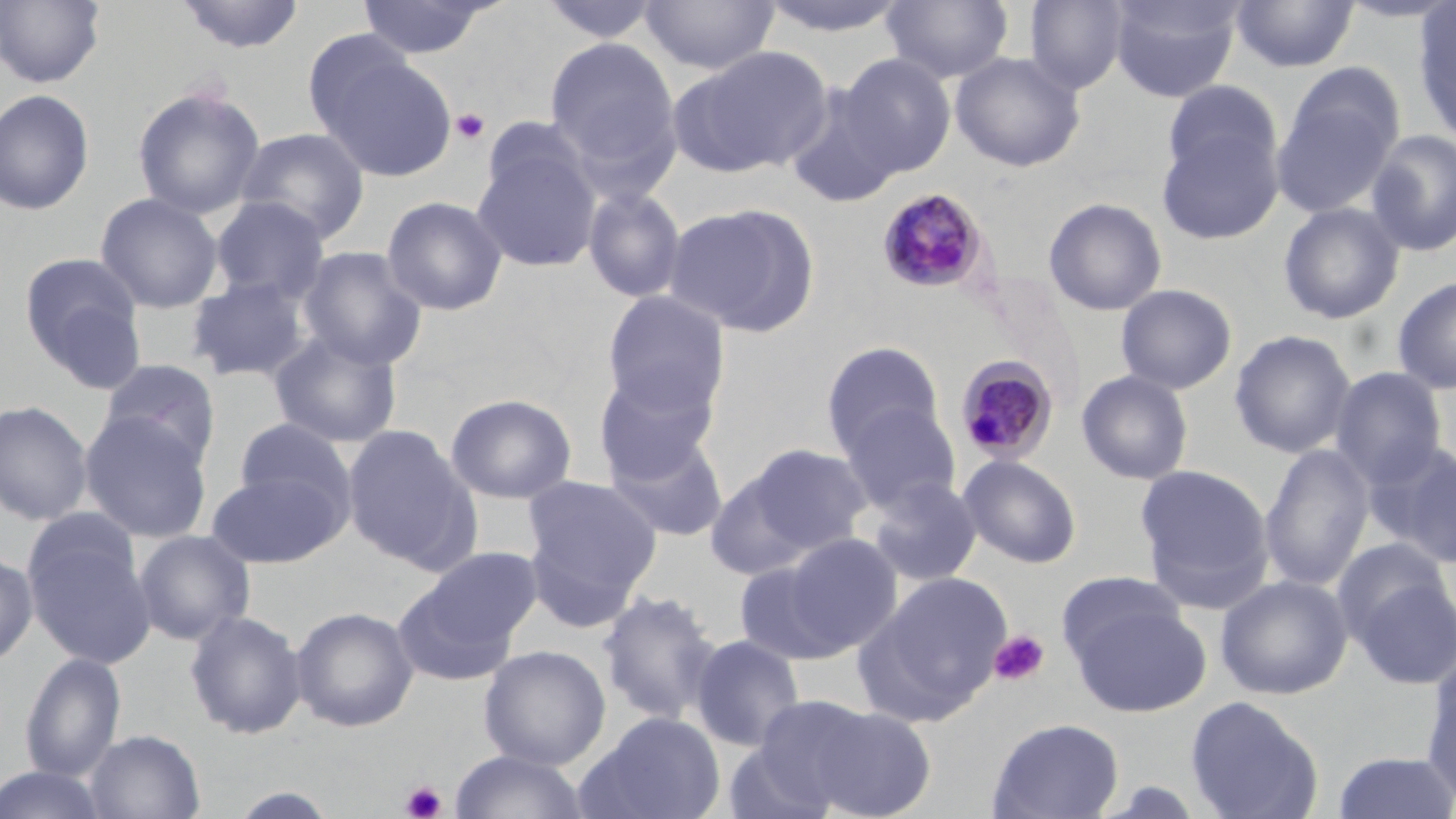

Summary:
  - Coordinate format: approximate bounding boxes as (x1,y1)-(x2,y2) corner pairs in pixels
  - Plasmodium malariae-infected red blood cell locations: (877,187)-(991,294), (954,354)-(1060,465)
  - Uninfected red blood cell locations: (0,0)-(106,88), (173,0)-(307,55), (356,0)-(497,60), (537,0)-(665,45), (640,0)-(780,76), (755,0)-(912,38), (881,0)-(1014,84), (1024,0)-(1130,94), (1108,0)-(1244,103), (1230,0)-(1359,72), (1412,2)-(1456,145), (544,36)-(682,182), (670,45)-(834,178), (319,51)-(458,182), (950,51)-(1086,172), (836,53)-(957,177), (1271,78)-(1400,219), (1160,80)-(1284,189), (131,85)-(266,219), (783,85)-(905,210), (0,89)-(96,215), (1156,121)-(1284,246), (236,126)-(370,243), (1366,129)-(1456,257), (471,137)-(603,273), (581,185)-(687,304), (95,192)-(223,313), (381,195)-(508,316), (210,196)-(329,303), (1043,197)-(1167,316), (664,202)-(821,337), (1278,202)-(1405,324), (298,246)-(429,369), (18,254)-(145,381), (184,275)-(314,385), (1392,276)-(1456,395), (1116,283)-(1238,395), (601,291)-(730,417), (268,330)-(403,449), (1230,330)-(1356,459), (820,340)-(946,459), (98,358)-(220,469), (594,367)-(721,483), (1330,367)-(1448,488), (1077,369)-(1194,485), (445,393)-(577,504), (0,400)-(94,526), (839,401)-(961,514), (79,412)-(213,543), (233,417)-(357,525), (341,424)-(476,568), (604,432)-(729,543), (1376,442)-(1456,567), (736,443)-(875,558), (1259,444)-(1375,593), (958,454)-(1082,569), (1135,463)-(1275,610), (206,469)-(346,568), (521,473)-(662,613), (866,476)-(983,586), (22,516)-(156,670), (132,529)-(256,645), (781,532)-(903,653), (1332,536)-(1452,648), (417,547)-(544,653), (0,550)-(38,668), (733,560)-(848,665), (1056,570)-(1187,667), (860,571)-(1012,723), (1350,571)-(1456,689), (1215,574)-(1353,700), (391,576)-(523,687), (597,589)-(722,725), (1070,602)-(1210,717), (290,606)-(420,732), (184,609)-(308,740), (689,633)-(808,752), (478,644)-(611,770), (20,651)-(126,782), (1421,657)-(1456,802), (744,695)-(883,814), (1185,695)-(1325,819), (795,702)-(939,819), (579,711)-(726,819), (986,717)-(1124,818), (85,729)-(206,819), (449,749)-(592,819), (1331,749)-(1455,819), (0,765)-(110,819), (225,786)-(343,819)
  - Platelet locations: (450,108)-(491,145), (989,630)-(1050,686), (400,780)-(447,819)
  - Slide-level diagnosis: Plasmodium malariae
  - Stain: May-Grünwald-Giemsa
  - Modality: optical microscopy
  - Image size: 1456×819 pixels
  - Field of view: single
  - Magnification: 1000x
  - Preparation: thin blood film